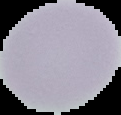
image size = 121×115 pixels
result = no Plasmodium parasites detected
preparation = thin blood film
image type = cell region segmented out of the field of view; surrounding area masked to black